Locate and identify every blood parasite.
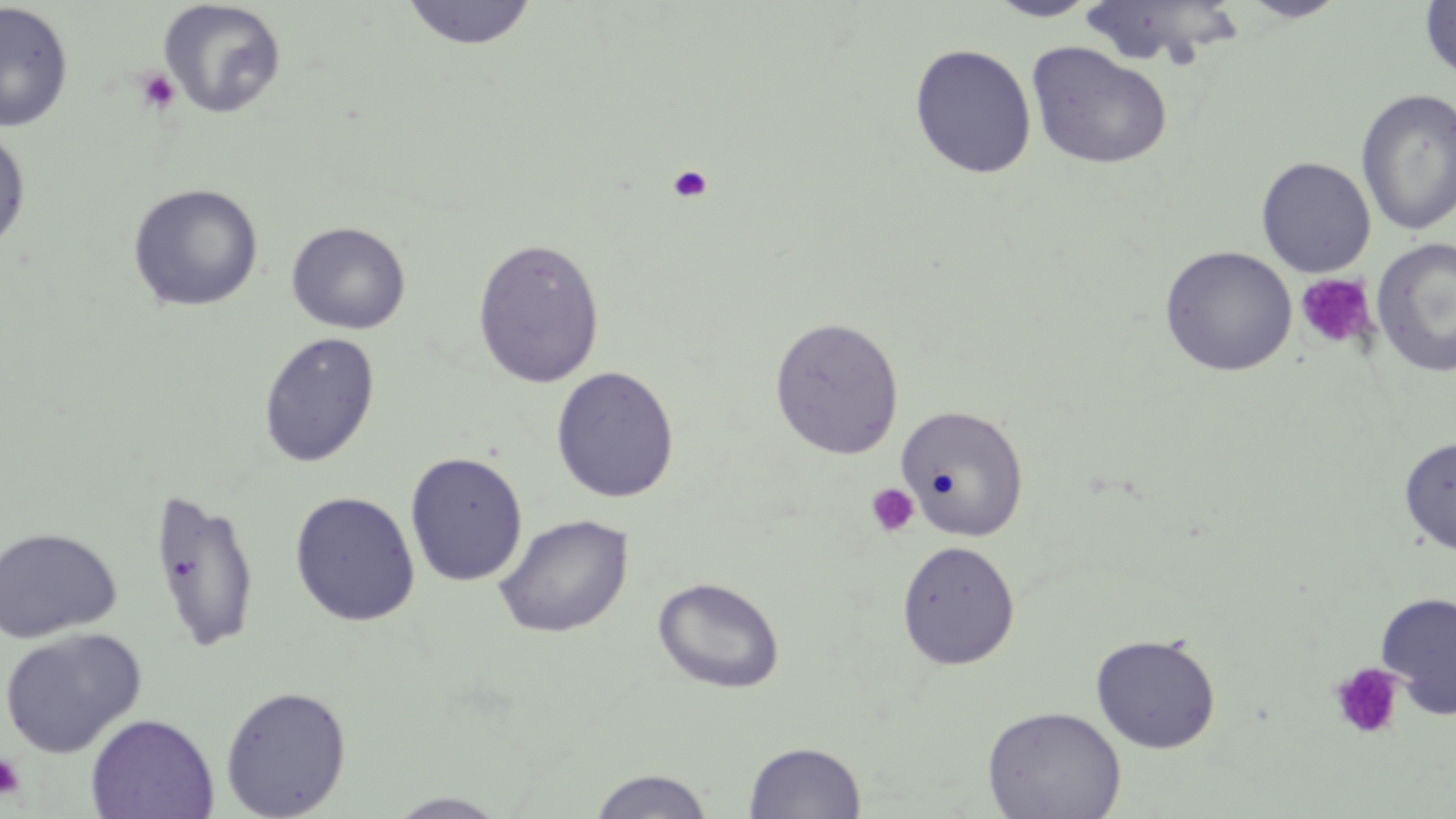
No blood parasites seen.

Approximate bounding boxes as (x1,y1)-(x2,y2) corner pairs in pixels. Platelet locations: (134,68)-(180,114), (667,165)-(713,204), (1295,273)-(1378,353), (864,483)-(920,538), (1329,663)-(1404,740), (0,753)-(26,800). Uninfected red blood cell locations: (400,0)-(538,50), (986,0)-(1102,22), (1238,0)-(1349,22), (157,1)-(287,119), (1420,1)-(1455,83), (0,2)-(74,133), (1073,2)-(1249,70), (1026,41)-(1173,170), (909,43)-(1037,179), (1355,88)-(1456,237), (0,128)-(31,253), (1256,157)-(1375,277), (126,182)-(264,312), (285,221)-(411,335), (1372,236)-(1456,380), (472,237)-(605,389), (1160,245)-(1297,377), (768,316)-(905,459), (257,332)-(381,468), (550,366)-(680,503), (896,404)-(1030,541), (1399,436)-(1456,556), (405,451)-(528,587), (148,486)-(261,654), (289,491)-(420,626), (493,514)-(633,638), (0,526)-(122,644), (896,540)-(1021,670), (653,576)-(785,693), (1375,591)-(1456,719), (0,627)-(146,757), (1090,632)-(1221,753), (219,685)-(352,819), (981,705)-(1126,819), (85,713)-(219,818), (743,740)-(867,819), (586,768)-(716,818), (385,791)-(513,818). Slide-level diagnosis: negative for blood parasites. Captured at 1000x magnification. Image is 1456×819 pixels. Single field of view. May-Grünwald-Giemsa-stained preparation. Thin blood smear. Light microscopy.